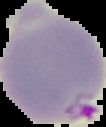
Summary:
  - Preparation: thin blood smear
  - Image size: 106×127 pixels
  - Result: Plasmodium parasites identified
  - Image type: segmented cell region with the area outside set to black